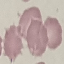 Result: negative for malaria parasites. Cell patch, automatically extracted from a larger field of view and resized to 64 × 64 pixels. Photographed with a smartphone camera at the microscope eyepiece. Thin blood smear. Giemsa stain.